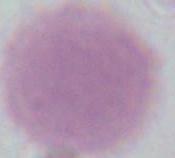 An erythrocyte is seen. Photomicrograph. 1000x magnification.